Report the malaria status of this cell.
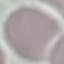

It is uninfected.

preparation = thin blood film
stain = Giemsa
capture = smartphone through the microscope eyepiece
image type = cell patch, automatically extracted from a larger field of view and resized to 64 × 64 pixels